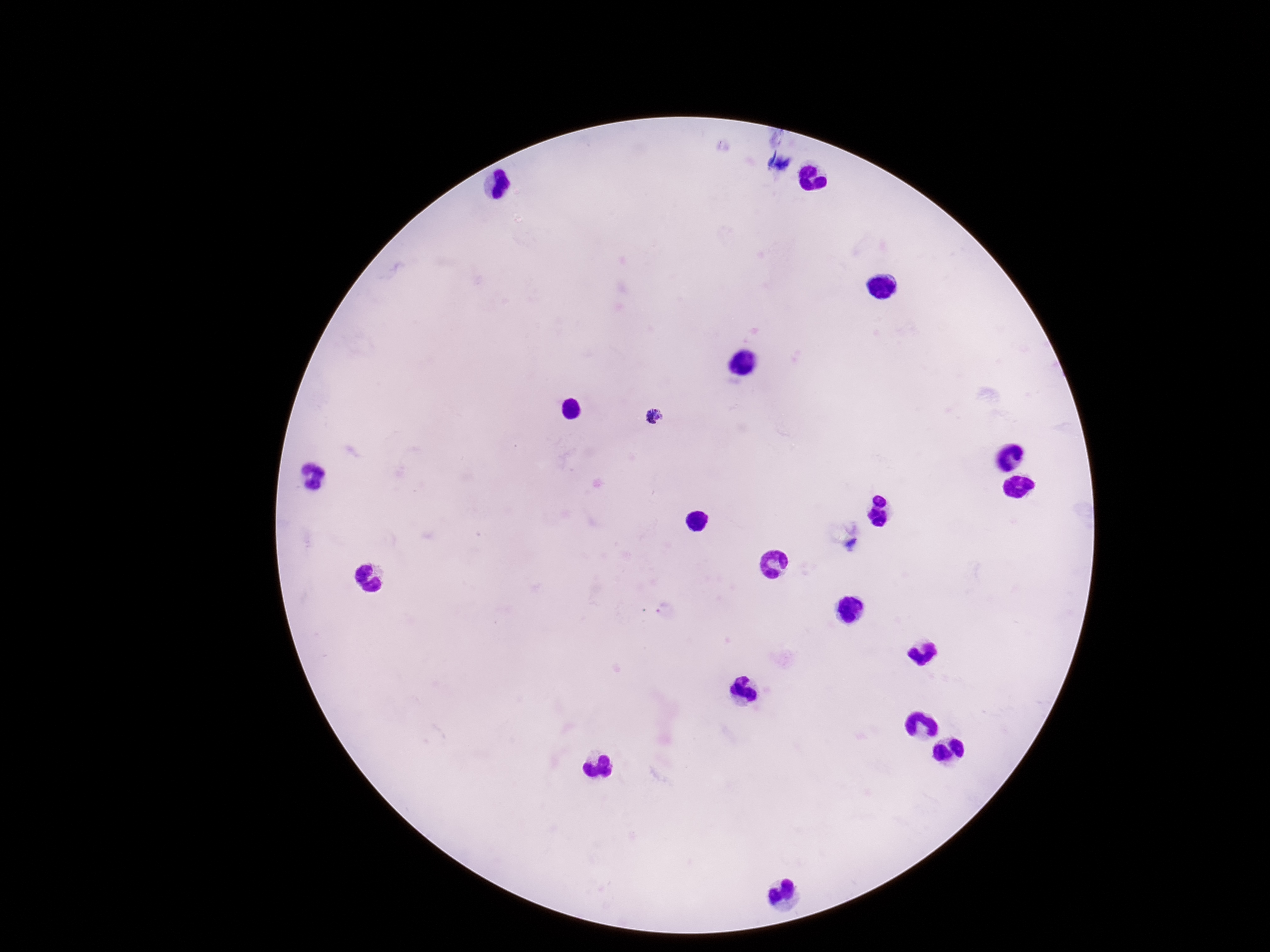
{
  "stain": "Giemsa",
  "patient_malaria_status": "infected",
  "magnification": "100x",
  "image_size": "1270×952 pixels",
  "preparation": "thick blood smear",
  "field_of_view": "one from this slide",
  "capture": "smartphone camera through the microscope eyepiece",
  "plasmodium_parasite_locations": "approximate centers as {x, y} in pixels: {653, 416}"
}